Identify the parasite.
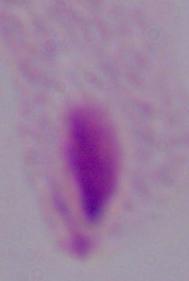

This is a trichomonad.

modality = micrograph
magnification = 1000x